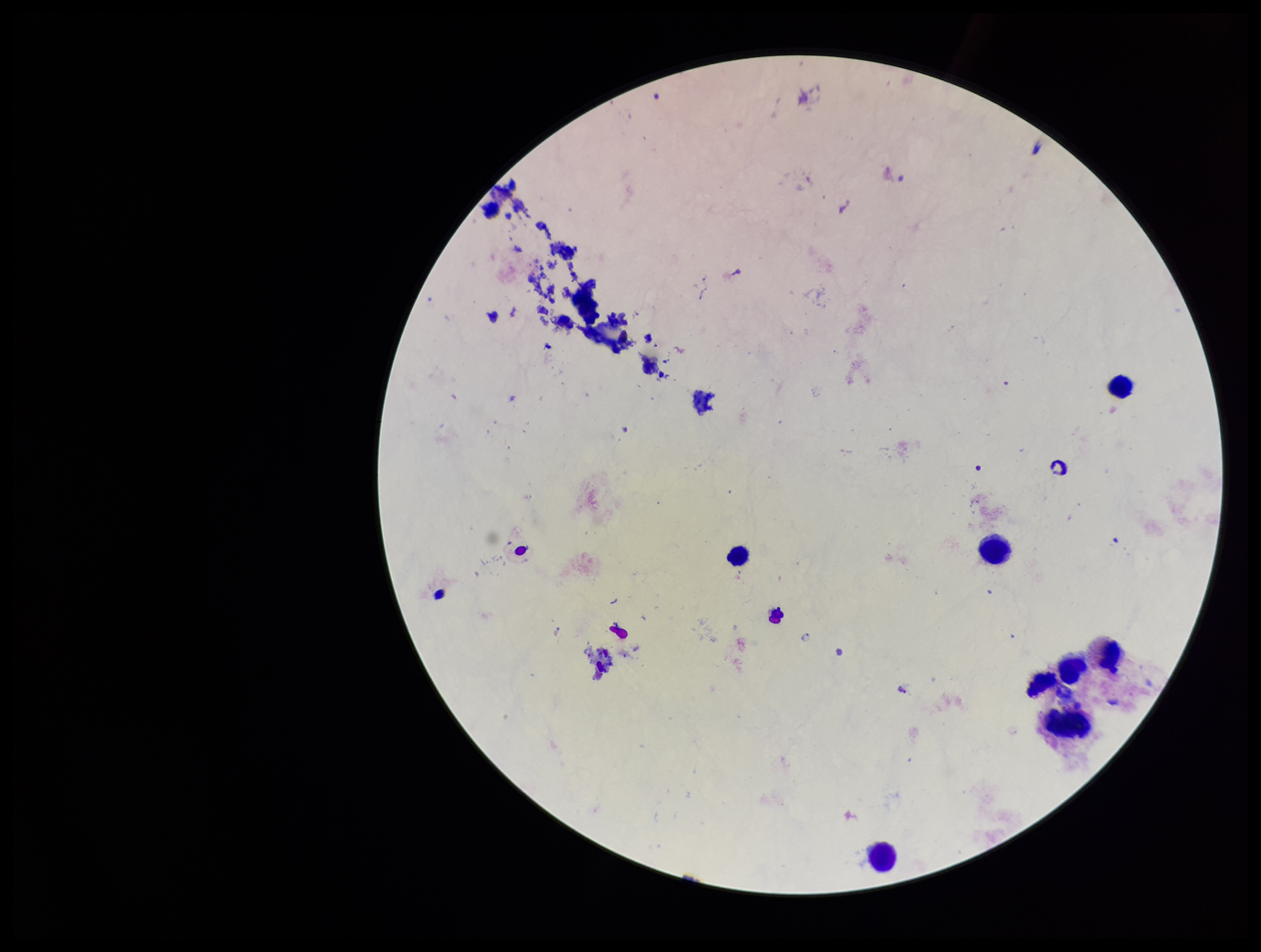
Photographed through the microscope eyepiece with a smartphone camera. Parasite count: 0. Preparation: thick smear. Patient malaria status: negative. Giemsa stain. Plasmodium parasites: none detected. Image is 1261×952 pixels. Leukocyte count: 9. One field from this slide.